Report the malaria status of this cell.
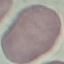

It is uninfected.

Summary:
  - Image type: cell patch, automatically extracted from a larger field of view and resized to 64 × 64 pixels
  - Stain: Giemsa
  - Capture: smartphone through the microscope eyepiece
  - Preparation: thin blood film